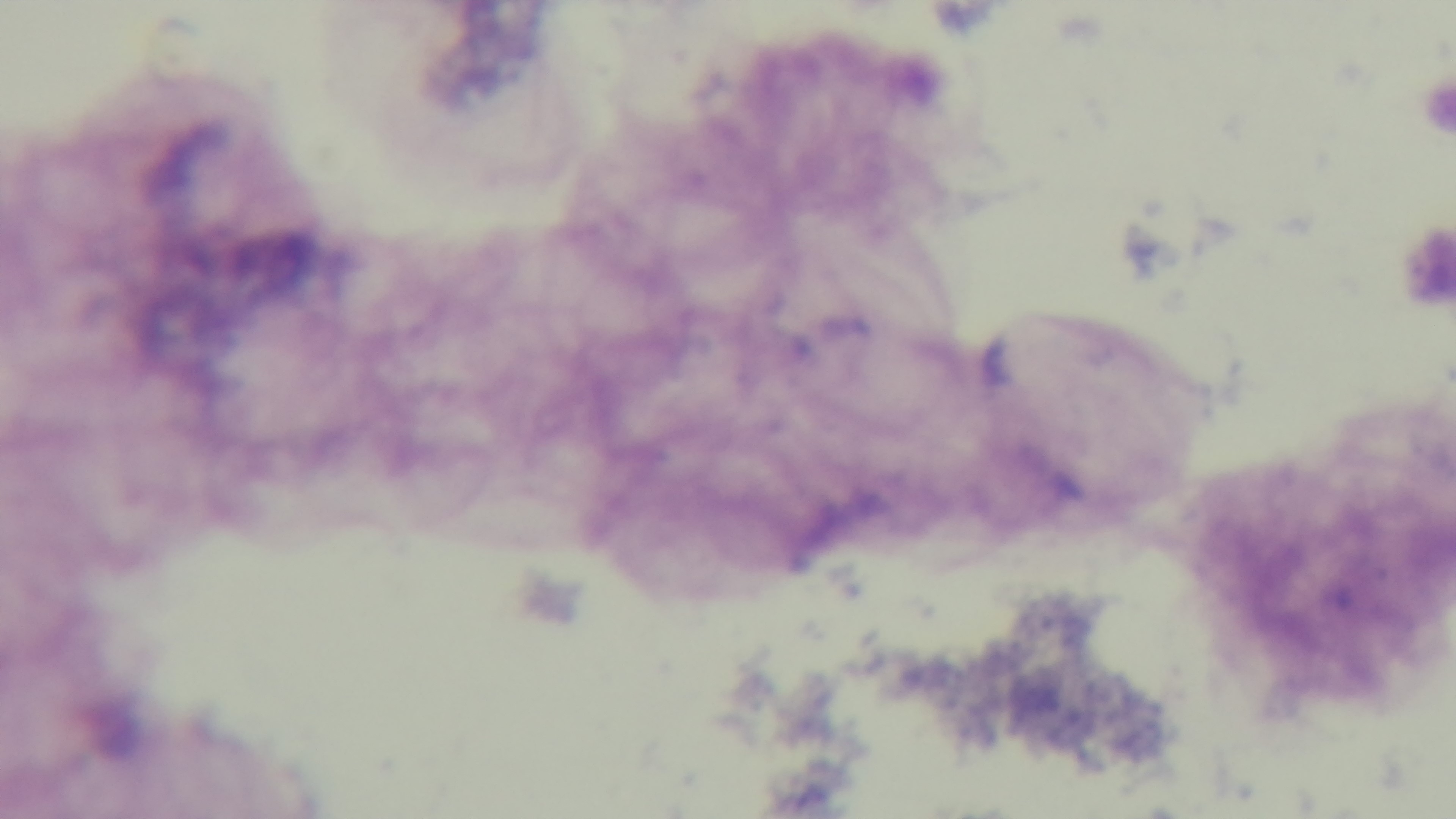

modality: light microscopy
malaria_status: uninfected
capture: mounted 4K digital camera
preparation: thick
objective: 100x oil immersion
stain: Giemsa
field_of_view: one from the slide